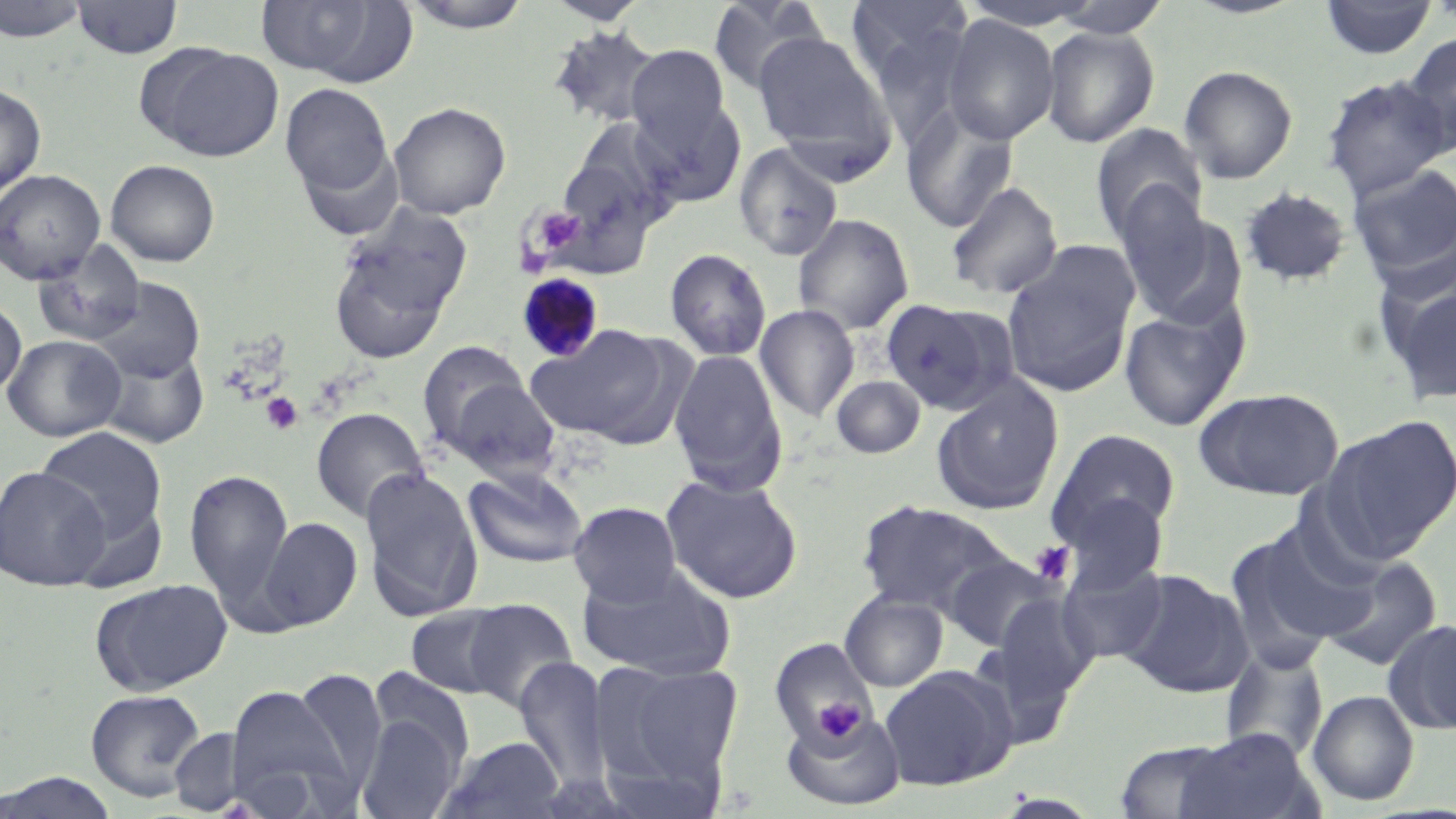
Approximate bounding boxes as named x1/y1/x2/y2 corners in pixels. Uninfected red blood cell locations: (x1=0, y1=0, x2=90, y2=43), (x1=72, y1=0, x2=182, y2=60), (x1=254, y1=0, x2=406, y2=81), (x1=399, y1=0, x2=536, y2=33), (x1=543, y1=0, x2=650, y2=25), (x1=706, y1=0, x2=829, y2=96), (x1=845, y1=0, x2=974, y2=105), (x1=1047, y1=0, x2=1172, y2=39), (x1=1319, y1=0, x2=1438, y2=60), (x1=956, y1=2, x2=1108, y2=31), (x1=941, y1=14, x2=1060, y2=145), (x1=548, y1=25, x2=664, y2=131), (x1=1040, y1=25, x2=1160, y2=148), (x1=751, y1=29, x2=896, y2=168), (x1=1399, y1=32, x2=1456, y2=156), (x1=138, y1=44, x2=286, y2=161), (x1=625, y1=45, x2=731, y2=152), (x1=1178, y1=64, x2=1299, y2=184), (x1=1321, y1=75, x2=1453, y2=200), (x1=280, y1=82, x2=395, y2=206), (x1=0, y1=83, x2=46, y2=202), (x1=631, y1=95, x2=747, y2=206), (x1=389, y1=101, x2=511, y2=219), (x1=901, y1=105, x2=1019, y2=234), (x1=566, y1=117, x2=683, y2=226), (x1=1091, y1=123, x2=1208, y2=243), (x1=733, y1=143, x2=844, y2=262), (x1=105, y1=159, x2=220, y2=267), (x1=551, y1=162, x2=656, y2=254), (x1=1347, y1=162, x2=1456, y2=279), (x1=0, y1=168, x2=106, y2=284), (x1=945, y1=180, x2=1064, y2=300), (x1=1238, y1=186, x2=1353, y2=288), (x1=1113, y1=193, x2=1235, y2=325), (x1=329, y1=213, x2=469, y2=360), (x1=792, y1=213, x2=914, y2=335), (x1=32, y1=241, x2=147, y2=348), (x1=1001, y1=246, x2=1139, y2=398), (x1=664, y1=248, x2=772, y2=361), (x1=1380, y1=272, x2=1456, y2=407), (x1=91, y1=278, x2=204, y2=383), (x1=0, y1=296, x2=27, y2=397), (x1=881, y1=298, x2=1011, y2=413), (x1=1118, y1=301, x2=1248, y2=432), (x1=754, y1=304, x2=860, y2=422), (x1=528, y1=325, x2=675, y2=445), (x1=3, y1=334, x2=126, y2=442), (x1=416, y1=341, x2=532, y2=454), (x1=96, y1=344, x2=211, y2=450), (x1=668, y1=349, x2=788, y2=496), (x1=831, y1=375, x2=925, y2=458), (x1=445, y1=377, x2=561, y2=481), (x1=931, y1=377, x2=1064, y2=516), (x1=1195, y1=387, x2=1344, y2=499), (x1=310, y1=407, x2=430, y2=524), (x1=1319, y1=415, x2=1456, y2=562), (x1=34, y1=425, x2=168, y2=551), (x1=1047, y1=428, x2=1182, y2=549), (x1=0, y1=466, x2=111, y2=590), (x1=359, y1=466, x2=484, y2=620), (x1=463, y1=466, x2=588, y2=569), (x1=184, y1=467, x2=294, y2=612), (x1=661, y1=473, x2=803, y2=604), (x1=1062, y1=492, x2=1170, y2=590), (x1=855, y1=499, x2=1017, y2=618), (x1=568, y1=501, x2=682, y2=607), (x1=256, y1=516, x2=362, y2=633), (x1=1227, y1=523, x2=1373, y2=663), (x1=944, y1=555, x2=1062, y2=652), (x1=1319, y1=555, x2=1443, y2=672), (x1=1058, y1=556, x2=1169, y2=665), (x1=578, y1=564, x2=736, y2=682), (x1=1119, y1=569, x2=1252, y2=698), (x1=89, y1=578, x2=232, y2=696), (x1=840, y1=591, x2=948, y2=692), (x1=988, y1=593, x2=1099, y2=709), (x1=461, y1=598, x2=579, y2=713), (x1=405, y1=604, x2=513, y2=698), (x1=1384, y1=619, x2=1456, y2=736), (x1=768, y1=637, x2=879, y2=751), (x1=1219, y1=645, x2=1330, y2=763), (x1=514, y1=658, x2=613, y2=792), (x1=592, y1=659, x2=744, y2=798), (x1=880, y1=665, x2=1017, y2=791), (x1=368, y1=666, x2=477, y2=772), (x1=291, y1=668, x2=387, y2=793), (x1=223, y1=683, x2=355, y2=813), (x1=85, y1=688, x2=207, y2=802), (x1=1307, y1=689, x2=1419, y2=806), (x1=780, y1=706, x2=906, y2=812), (x1=356, y1=710, x2=464, y2=819), (x1=168, y1=727, x2=248, y2=815), (x1=1173, y1=729, x2=1315, y2=819), (x1=437, y1=735, x2=567, y2=819), (x1=1112, y1=739, x2=1240, y2=818), (x1=0, y1=770, x2=124, y2=817). Platelet locations: (x1=536, y1=208, x2=585, y2=252), (x1=260, y1=392, x2=304, y2=436), (x1=1030, y1=542, x2=1074, y2=585), (x1=813, y1=698, x2=862, y2=744). Plasmodium malariae-infected red blood cell locations: (x1=516, y1=273, x2=606, y2=363). Slide-level diagnosis: Plasmodium malariae. Image is 1456×819 pixels. Single field of view. Captured at 1000x magnification. Optical microscopy. Thin blood film. May-Grünwald-Giemsa stain.